Point out each Plasmodium parasite.
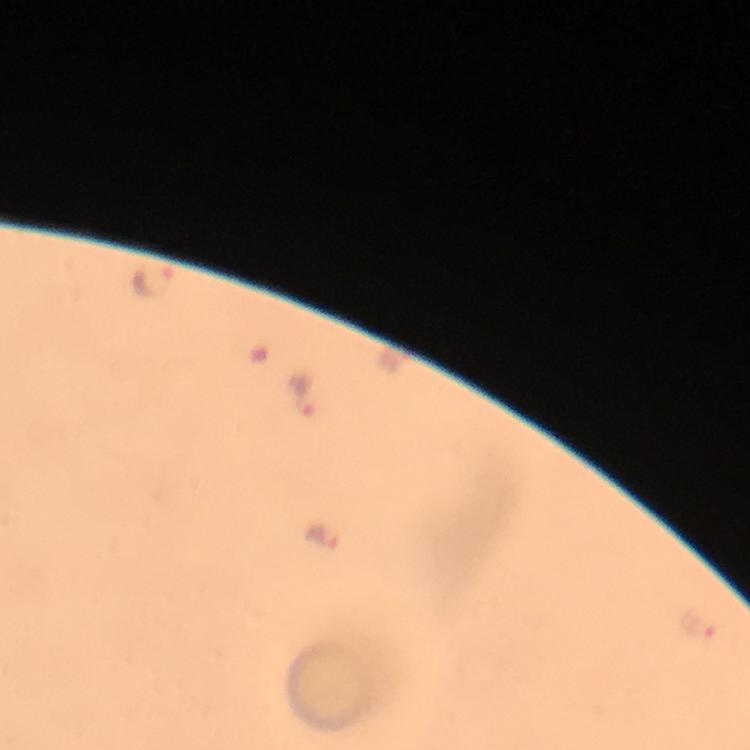
Approximate centers as [x, y] in pixels.
Plasmodium parasites: [152, 278], [300, 393], [322, 533], [701, 626].

{
  "preparation": "thick blood smear",
  "capture": "smartphone camera through the microscope",
  "context": "from a diagnostic examination for malaria",
  "stain": "Giemsa",
  "magnification": "100x",
  "immersion_oil": "applied",
  "image_size": "750×750 pixels",
  "cropped_from": "a single field of view"
}